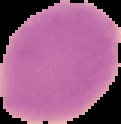
{
  "result": "no malaria parasites detected",
  "image_size": "121×124 pixels",
  "image_type": "cell region segmented out of the field of view; surrounding area masked to black",
  "preparation": "thin blood film"
}